Give the extent of all Plasmodium falciparum-infected red blood cells.
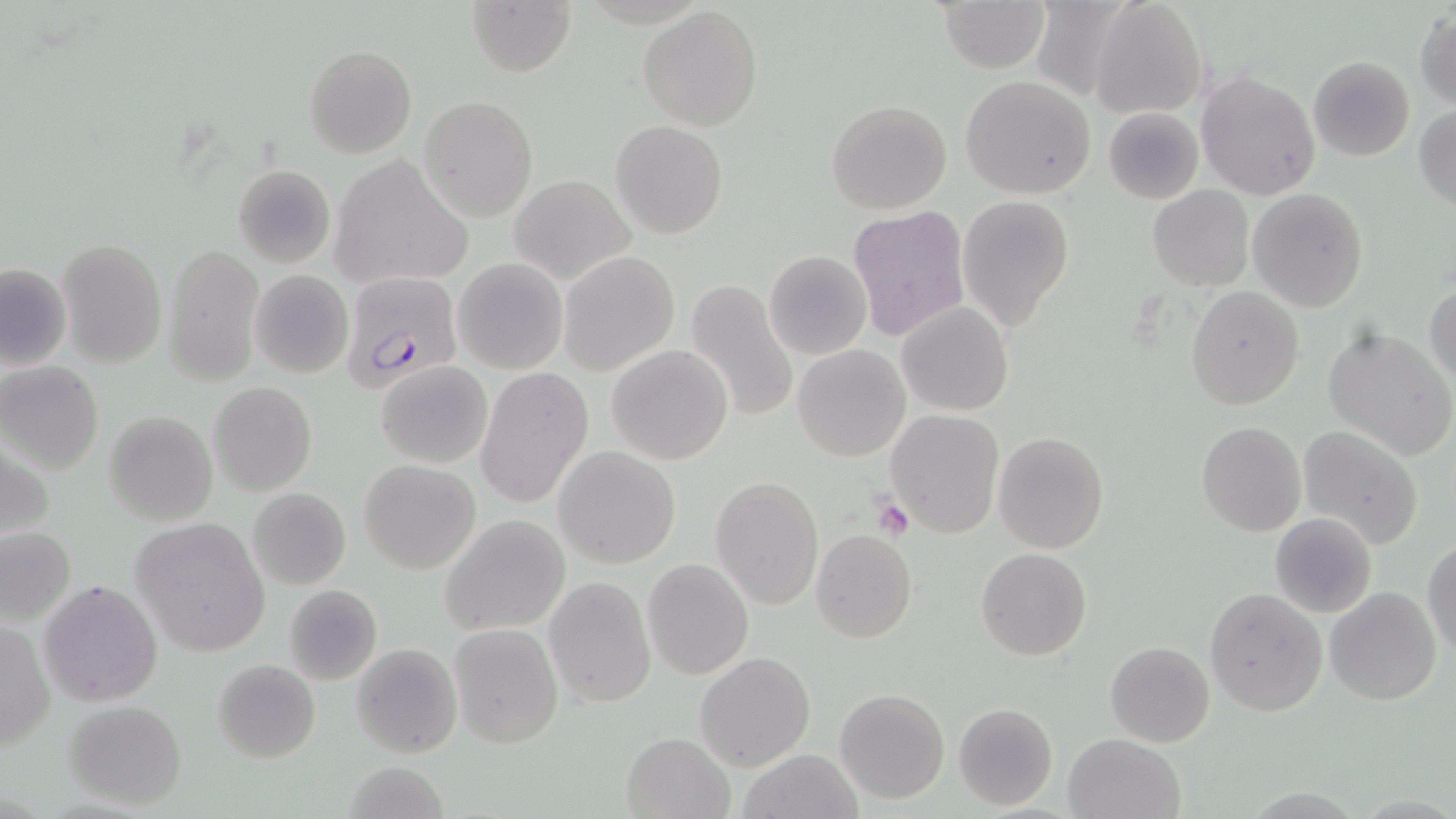
Approximate bounding boxes as (x1,y1)-(x2,y2) corner pairs in pixels.
Plasmodium falciparum-infected red blood cells: (344,273)-(464,411).

{
  "slide_level_diagnosis": "Plasmodium falciparum",
  "stain": "May-Grünwald-Giemsa",
  "uninfected_red_blood_cell_locations": "approximate bounding boxes as (x1,y1)-(x2,y2) corner pairs in pixels: (1091,0)-(1208,119), (466,1)-(577,78), (939,1)-(1049,73), (636,6)-(763,130), (1414,8)-(1456,111), (303,44)-(416,158), (1307,55)-(1414,161), (1196,70)-(1320,201), (959,76)-(1098,202), (419,95)-(538,221), (827,100)-(951,214), (1413,105)-(1456,214), (1103,106)-(1203,206), (611,119)-(729,238), (328,153)-(474,289), (233,163)-(335,268), (510,176)-(634,284), (1148,186)-(1254,293), (1246,189)-(1369,313), (956,196)-(1073,332), (846,205)-(969,344), (57,237)-(167,368), (163,244)-(263,385), (765,251)-(871,359), (559,252)-(679,375), (453,257)-(568,375), (0,262)-(72,373), (250,270)-(353,378), (685,280)-(799,424), (1425,283)-(1456,387), (1186,287)-(1305,410), (896,302)-(1014,417), (1324,328)-(1456,461), (607,345)-(733,464), (792,345)-(910,462), (375,360)-(493,470), (0,362)-(105,476), (478,366)-(594,509), (209,383)-(316,496), (884,409)-(1004,540), (104,410)-(218,526), (1196,421)-(1306,537), (1296,425)-(1425,548), (992,431)-(1109,554), (555,447)-(679,569), (358,458)-(480,575), (712,475)-(824,611), (248,490)-(351,587), (1269,512)-(1378,619), (438,515)-(570,637), (132,516)-(272,657), (0,525)-(77,626), (811,530)-(917,644), (1424,536)-(1456,659), (975,548)-(1092,661), (644,558)-(753,679), (544,577)-(655,707), (39,579)-(163,706), (283,584)-(383,685), (1324,586)-(1442,706), (1204,588)-(1327,716), (2,616)-(53,758), (448,622)-(563,749), (1104,641)-(1215,749), (352,643)-(462,758), (696,652)-(815,770), (213,658)-(320,763), (834,687)-(951,804), (63,699)-(187,811), (953,702)-(1058,810), (621,731)-(732,817), (1063,733)-(1186,819), (737,748)-(864,819), (338,763)-(452,818)",
  "platelet_locations": "approximate bounding boxes as (x1,y1)-(x2,y2) corner pairs in pixels: (872,495)-(914,538)",
  "modality": "optical microscopy",
  "preparation": "thin blood smear",
  "field_of_view": "single",
  "image_size": "1456×819 pixels",
  "magnification": "1000x"
}